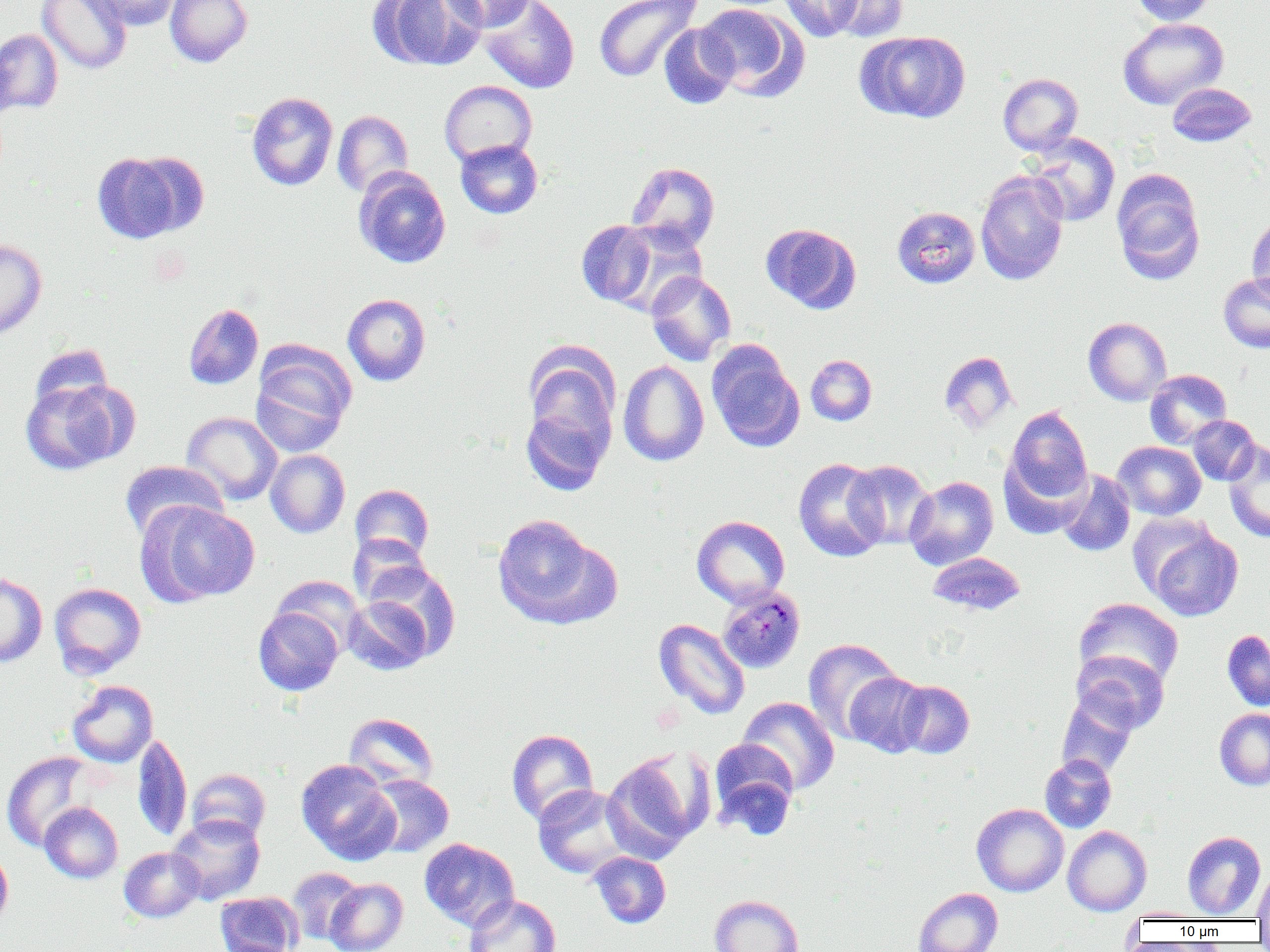
Summary:
  - Coordinate format: approximate bounding boxes as named x1/y1/x2/y2 corners in pixels
  - Uninfected red blood cell locations: (x1=37, y1=0, x2=132, y2=74), (x1=85, y1=0, x2=181, y2=31), (x1=165, y1=0, x2=252, y2=67), (x1=371, y1=0, x2=486, y2=70), (x1=443, y1=0, x2=536, y2=33), (x1=480, y1=0, x2=579, y2=93), (x1=593, y1=0, x2=702, y2=83), (x1=780, y1=0, x2=864, y2=41), (x1=827, y1=0, x2=909, y2=42), (x1=1131, y1=0, x2=1217, y2=25), (x1=696, y1=3, x2=807, y2=101), (x1=1118, y1=18, x2=1229, y2=109), (x1=658, y1=22, x2=739, y2=109), (x1=0, y1=29, x2=64, y2=114), (x1=857, y1=30, x2=970, y2=123), (x1=0, y1=43, x2=17, y2=123), (x1=998, y1=73, x2=1083, y2=155), (x1=439, y1=80, x2=537, y2=166), (x1=1167, y1=82, x2=1257, y2=147), (x1=247, y1=92, x2=338, y2=191), (x1=332, y1=110, x2=413, y2=198), (x1=1027, y1=133, x2=1120, y2=227), (x1=455, y1=139, x2=543, y2=218), (x1=92, y1=151, x2=196, y2=243), (x1=626, y1=161, x2=720, y2=251), (x1=353, y1=167, x2=451, y2=268), (x1=1111, y1=170, x2=1205, y2=283), (x1=975, y1=171, x2=1069, y2=285), (x1=892, y1=206, x2=980, y2=288), (x1=1247, y1=215, x2=1270, y2=307), (x1=576, y1=220, x2=658, y2=307), (x1=608, y1=223, x2=708, y2=318), (x1=761, y1=223, x2=861, y2=314), (x1=0, y1=238, x2=47, y2=340), (x1=646, y1=271, x2=736, y2=366), (x1=1218, y1=272, x2=1270, y2=353), (x1=342, y1=293, x2=431, y2=386), (x1=183, y1=303, x2=264, y2=390), (x1=1083, y1=317, x2=1172, y2=406), (x1=251, y1=343, x2=355, y2=458), (x1=524, y1=343, x2=621, y2=449), (x1=29, y1=344, x2=113, y2=416), (x1=707, y1=344, x2=804, y2=451), (x1=939, y1=351, x2=1018, y2=434), (x1=805, y1=354, x2=877, y2=426), (x1=618, y1=360, x2=709, y2=466), (x1=1144, y1=369, x2=1232, y2=449), (x1=20, y1=379, x2=133, y2=475), (x1=520, y1=400, x2=614, y2=496), (x1=1002, y1=405, x2=1093, y2=513), (x1=182, y1=411, x2=282, y2=505), (x1=1187, y1=415, x2=1260, y2=485), (x1=1112, y1=441, x2=1206, y2=520), (x1=1224, y1=441, x2=1270, y2=543), (x1=265, y1=449, x2=350, y2=538), (x1=793, y1=457, x2=888, y2=562), (x1=119, y1=460, x2=228, y2=542), (x1=844, y1=460, x2=935, y2=549), (x1=1055, y1=468, x2=1136, y2=557), (x1=904, y1=475, x2=999, y2=569), (x1=350, y1=484, x2=434, y2=563), (x1=137, y1=502, x2=260, y2=605), (x1=492, y1=514, x2=616, y2=629), (x1=692, y1=515, x2=790, y2=607), (x1=1144, y1=525, x2=1243, y2=621), (x1=348, y1=534, x2=433, y2=607), (x1=926, y1=552, x2=1026, y2=617), (x1=0, y1=572, x2=47, y2=668), (x1=271, y1=575, x2=364, y2=655), (x1=49, y1=582, x2=146, y2=678), (x1=342, y1=590, x2=438, y2=675), (x1=1074, y1=598, x2=1183, y2=690), (x1=253, y1=605, x2=345, y2=696), (x1=654, y1=618, x2=750, y2=720), (x1=1221, y1=629, x2=1270, y2=712), (x1=802, y1=638, x2=902, y2=743), (x1=1070, y1=650, x2=1170, y2=735), (x1=844, y1=671, x2=930, y2=757), (x1=896, y1=679, x2=975, y2=759), (x1=67, y1=680, x2=158, y2=767), (x1=1056, y1=692, x2=1141, y2=778), (x1=737, y1=696, x2=840, y2=795), (x1=1214, y1=708, x2=1270, y2=790), (x1=344, y1=713, x2=439, y2=791), (x1=506, y1=729, x2=599, y2=826), (x1=131, y1=733, x2=192, y2=842), (x1=709, y1=738, x2=799, y2=836), (x1=601, y1=749, x2=709, y2=861), (x1=1, y1=751, x2=98, y2=852), (x1=1040, y1=754, x2=1117, y2=832), (x1=296, y1=759, x2=400, y2=864), (x1=187, y1=768, x2=271, y2=843), (x1=365, y1=774, x2=454, y2=857), (x1=533, y1=784, x2=635, y2=879), (x1=40, y1=802, x2=123, y2=883), (x1=972, y1=803, x2=1069, y2=896), (x1=168, y1=813, x2=265, y2=904), (x1=1062, y1=826, x2=1151, y2=916), (x1=1183, y1=831, x2=1266, y2=919), (x1=419, y1=838, x2=520, y2=931), (x1=0, y1=846, x2=13, y2=932), (x1=119, y1=847, x2=204, y2=922), (x1=588, y1=851, x2=671, y2=928), (x1=1253, y1=866, x2=1270, y2=922), (x1=286, y1=867, x2=364, y2=946), (x1=324, y1=878, x2=408, y2=952), (x1=912, y1=887, x2=1003, y2=952), (x1=215, y1=891, x2=303, y2=952), (x1=464, y1=894, x2=562, y2=952), (x1=709, y1=895, x2=804, y2=952), (x1=1121, y1=907, x2=1212, y2=921)
  - Plasmodium malariae-infected red blood cell locations: (x1=717, y1=585, x2=806, y2=674)
  - Slide-level diagnosis: Plasmodium malariae
  - Image size: 1270×952 pixels
  - Field of view: single
  - Preparation: thin blood film
  - Modality: light microscopy
  - Magnification: 1000x